Comment on the morphology of the erythrocytes.
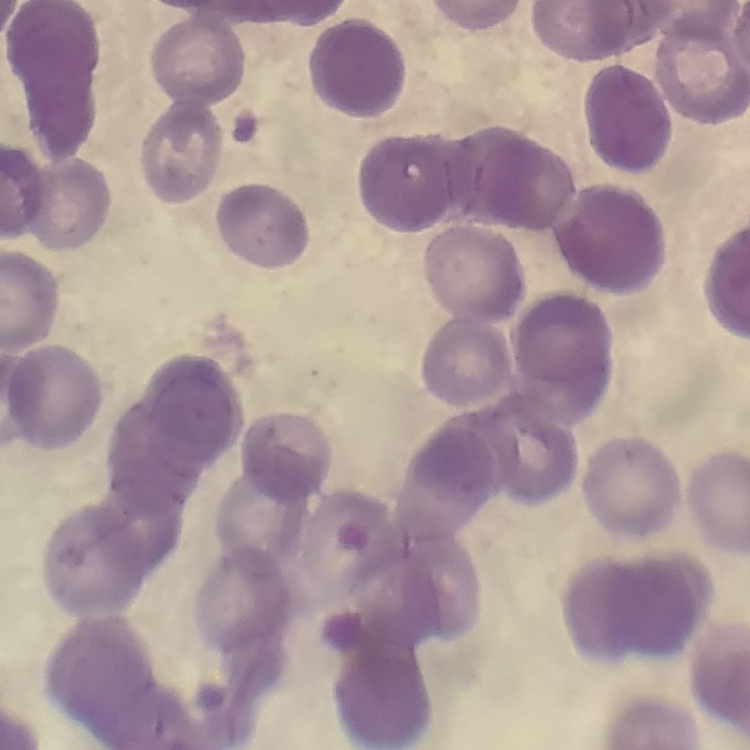
They show rouleaux formation.

stain: Field's or Giemsa
image_type: square crop of a larger photomicrograph
preparation: thin blood film